State the blood parasite species.
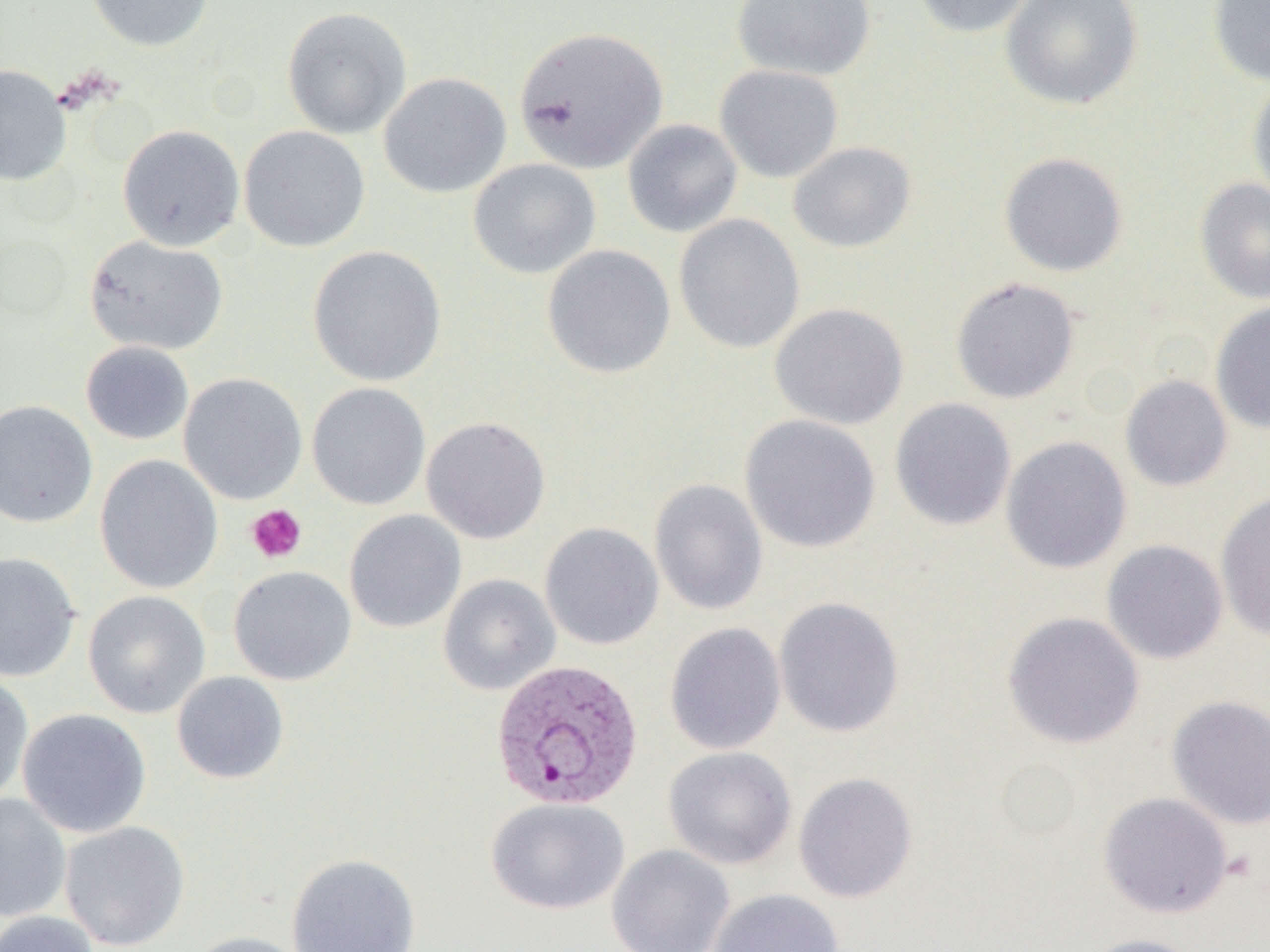
Plasmodium vivax.

field_of_view: one of a larger specimen
platelet_locations: 'approximate bounding boxes as (x1,y1)-(x2,y2) corner pairs in pixels: (245,505)-(307,564)'
image_size: 1270×952 pixels
preparation: thin blood film
magnification: 1000x
uninfected_red_blood_cell_locations: 'approximate bounding boxes as (x1,y1)-(x2,y2) corner pairs in pixels: (85,0)-(214,52), (732,0)-(877,82), (910,0)-(1038,38), (1001,0)-(1144,110), (1207,0)-(1270,85), (282,7)-(412,139), (513,26)-(668,173), (0,64)-(71,186), (714,64)-(844,183), (378,72)-(511,198), (1247,77)-(1270,206), (622,119)-(743,238), (117,124)-(244,251), (238,125)-(370,252), (787,141)-(917,253), (999,151)-(1128,277), (468,158)-(601,278), (1194,177)-(1270,305), (673,213)-(805,354), (84,235)-(229,356), (541,244)-(676,379), (308,245)-(446,387), (950,276)-(1080,405), (1210,301)-(1270,434), (769,303)-(909,430), (80,341)-(194,445), (178,373)-(308,505), (1120,375)-(1233,491), (306,383)-(431,510), (889,397)-(1016,531), (0,400)-(98,528), (739,414)-(881,553), (421,416)-(551,544), (1000,435)-(1132,574), (94,454)-(223,595), (649,478)-(769,615), (1215,491)-(1270,641), (344,510)-(466,633), (539,522)-(664,650), (1100,539)-(1229,665), (0,552)-(81,682), (228,565)-(357,685), (438,574)-(560,695), (82,590)-(211,719), (773,596)-(905,738), (1002,611)-(1144,749), (664,622)-(786,755), (0,671)-(34,807), (171,671)-(289,784), (1166,694)-(1270,829), (17,708)-(151,838), (663,746)-(797,869), (793,772)-(918,903), (1098,791)-(1233,918), (0,793)-(72,922), (485,797)-(630,915), (59,820)-(190,950), (606,844)-(735,952), (286,852)-(421,952), (707,888)-(843,952), (0,910)-(101,952), (182,931)-(313,952), (1080,933)-(1205,952)'
plasmodium_vivax_infected_red_blood_cell_locations: 'approximate bounding boxes as (x1,y1)-(x2,y2) corner pairs in pixels: (490,658)-(644,811)'
modality: light microscopy